Assess the background quality.
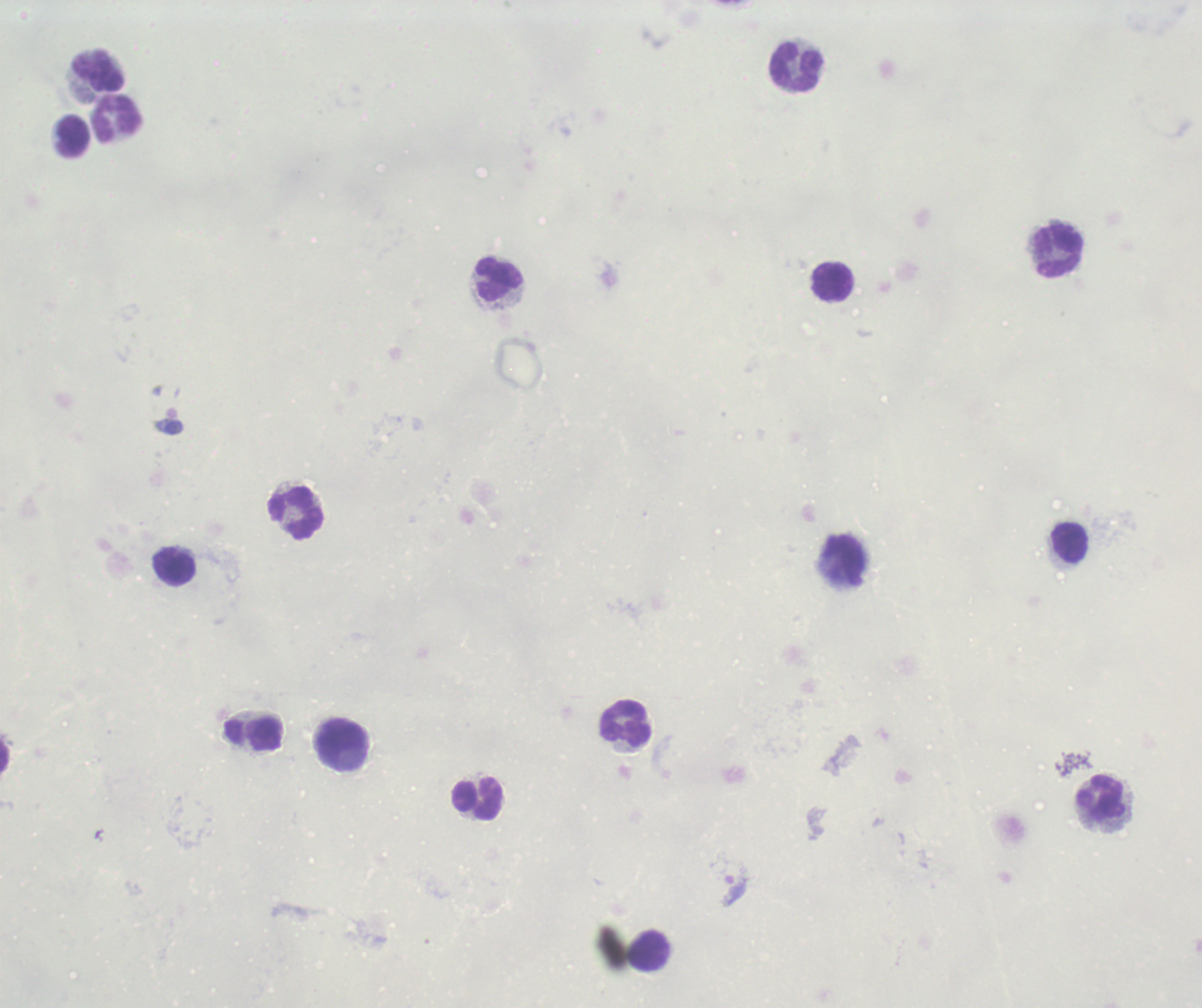
Poor.

{
  "result": "Plasmodium parasites detected",
  "field_of_view": "single",
  "image_size": "1202×1008 pixels",
  "trophozoite_locations": "approximate centers as (x, y) in pixels: (734, 891)",
  "context": "previously used in a real diagnosis",
  "magnification": "100x",
  "stain": "Romanowsky",
  "preparation": "thick smear of blood",
  "leukocyte_locations": "approximate centers as (x, y) in pixels: (796, 67), (97, 71), (117, 119), (73, 136), (1059, 251), (499, 279), (831, 281), (295, 514), (1069, 544), (846, 560), (174, 567), (626, 722), (254, 734), (341, 743), (1101, 799), (477, 800), (649, 952)"
}